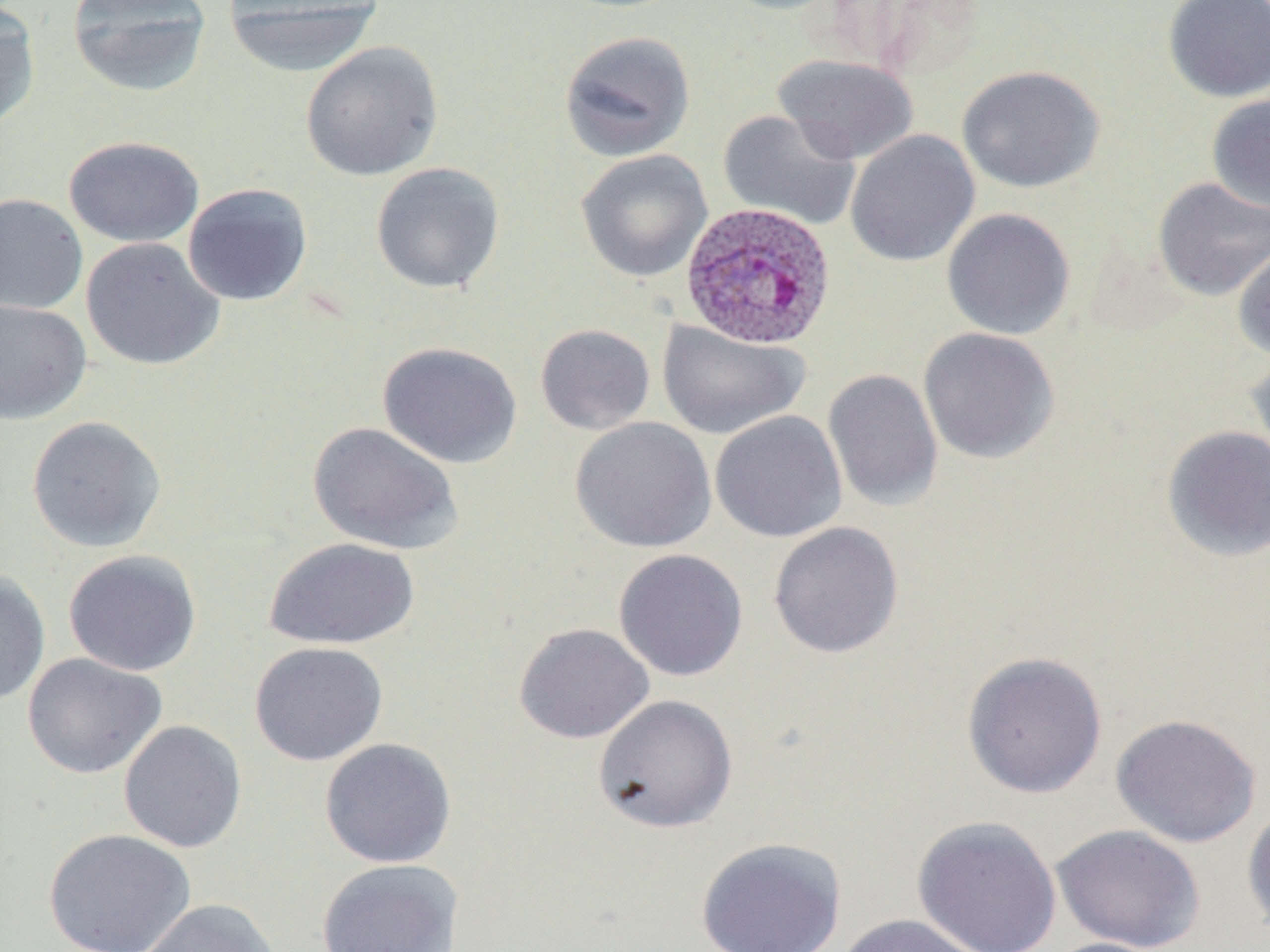

Summary:
  - Coordinate format: approximate bounding boxes as (x1, y1, x2, y2) in pixels
  - Uninfected red blood cell locations: (67, 0, 212, 97), (221, 0, 383, 77), (716, 0, 850, 16), (819, 0, 984, 78), (1162, 0, 1270, 102), (0, 2, 42, 134), (558, 30, 696, 162), (300, 41, 444, 181), (773, 54, 918, 164), (956, 65, 1105, 193), (1206, 93, 1270, 214), (718, 110, 861, 230), (845, 130, 980, 267), (63, 135, 205, 247), (575, 149, 713, 283), (370, 161, 505, 294), (1152, 177, 1270, 301), (182, 182, 313, 306), (0, 193, 88, 315), (941, 208, 1076, 340), (80, 237, 225, 371), (1232, 242, 1270, 362), (0, 299, 91, 424), (657, 320, 810, 439), (534, 323, 656, 435), (917, 327, 1060, 464), (377, 341, 523, 469), (1245, 350, 1270, 474), (823, 368, 944, 512), (709, 411, 847, 543), (26, 415, 167, 552), (569, 417, 717, 553), (308, 421, 462, 554), (1160, 424, 1270, 563), (768, 521, 904, 659), (263, 537, 420, 650), (612, 548, 748, 681), (63, 549, 201, 677), (0, 568, 51, 707), (513, 623, 655, 744), (249, 641, 388, 766), (962, 651, 1108, 798), (22, 653, 167, 779), (592, 694, 738, 833), (1110, 713, 1262, 848), (118, 720, 247, 853), (319, 737, 457, 868), (1241, 802, 1270, 938), (911, 815, 1063, 952), (1051, 824, 1205, 951), (43, 828, 196, 952), (695, 837, 846, 952), (316, 858, 463, 952), (137, 899, 280, 952), (835, 914, 989, 952), (1039, 937, 1173, 952)
  - Plasmodium ovale-infected red blood cell locations: (679, 201, 837, 350)
  - Slide-level diagnosis: Plasmodium ovale
  - Magnification: 1000x
  - Field of view: one of a larger specimen
  - Stain: May-Grünwald-Giemsa
  - Image size: 1270×952 pixels
  - Preparation: thin blood smear
  - Modality: optical microscopy